Locate every blood parasite and identify its species.
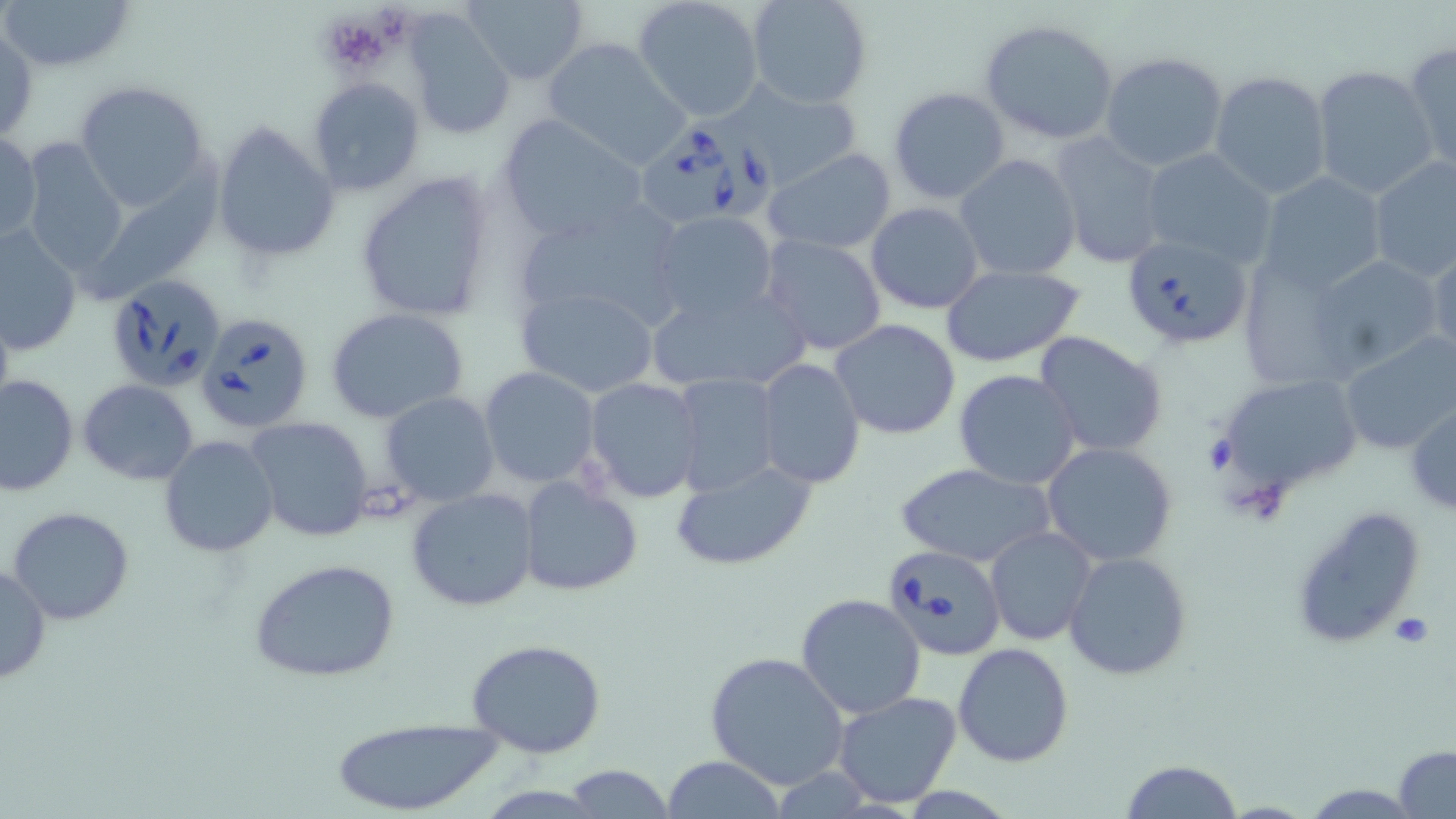
Approximate bounding boxes as [x1, y1, x2, y2] in pixels.
Babesia divergens-infected red blood cells: [634, 121, 775, 227], [1119, 234, 1253, 352], [102, 274, 227, 393], [194, 310, 316, 435], [880, 543, 1008, 661].
No Plasmodium falciparum, Plasmodium ovale, Plasmodium malariae, Plasmodium vivax, or Trypanosoma brucei observed.

slide-level diagnosis = Babesia divergens
platelet locations = approximate bounding boxes as [x1, y1, x2, y2] in pixels: [317, 7, 398, 80]
uninfected red blood cell locations = approximate bounding boxes as [x1, y1, x2, y2] in pixels: [1, 0, 135, 74], [463, 0, 589, 84], [633, 0, 765, 123], [747, 0, 874, 110], [404, 10, 516, 143], [977, 17, 1122, 147], [1, 25, 38, 144], [540, 38, 691, 170], [1404, 40, 1455, 176], [1100, 51, 1229, 173], [1310, 65, 1438, 199], [1209, 70, 1332, 199], [307, 75, 426, 196], [72, 80, 212, 213], [726, 83, 864, 191], [887, 87, 1011, 206], [497, 114, 651, 243], [212, 121, 339, 265], [1, 130, 41, 245], [1048, 132, 1172, 269], [18, 137, 132, 280], [763, 148, 897, 254], [1138, 148, 1280, 268], [954, 154, 1081, 280], [1367, 155, 1456, 283], [79, 158, 231, 312], [353, 169, 496, 325], [1255, 171, 1388, 295], [514, 198, 691, 338], [866, 201, 984, 314], [652, 211, 779, 325], [2, 225, 84, 355], [759, 233, 889, 357], [1426, 239, 1456, 368], [1302, 253, 1445, 378], [1230, 255, 1375, 389], [938, 264, 1086, 366], [515, 284, 663, 398], [644, 284, 817, 395], [325, 307, 471, 425], [830, 319, 963, 440], [1338, 331, 1456, 453], [1033, 333, 1168, 459], [756, 358, 865, 487], [479, 366, 600, 486], [953, 369, 1082, 490], [670, 372, 782, 497], [1211, 372, 1365, 506], [1, 373, 78, 496], [583, 378, 704, 503], [79, 379, 199, 485], [379, 391, 500, 506], [1407, 400, 1456, 517], [243, 416, 377, 542], [158, 435, 278, 558], [1041, 442, 1178, 567], [670, 457, 818, 572], [896, 461, 1055, 567], [516, 474, 641, 598], [406, 487, 539, 612], [1288, 503, 1427, 653], [8, 506, 132, 626], [986, 526, 1098, 646], [1063, 552, 1191, 681], [249, 558, 402, 685], [0, 562, 50, 686], [796, 593, 926, 721], [465, 636, 608, 757], [953, 643, 1074, 768], [705, 652, 849, 788], [831, 691, 963, 809], [329, 717, 502, 818], [1394, 745, 1456, 817], [660, 756, 788, 817], [1120, 759, 1242, 819], [564, 765, 673, 818], [1300, 783, 1425, 816]
image size = 1456×819 pixels
magnification = 1000x
stain = May-Grünwald-Giemsa
preparation = thin blood smear
modality = light microscopy
field of view = single